Give the extent of all uninfected red blood cells.
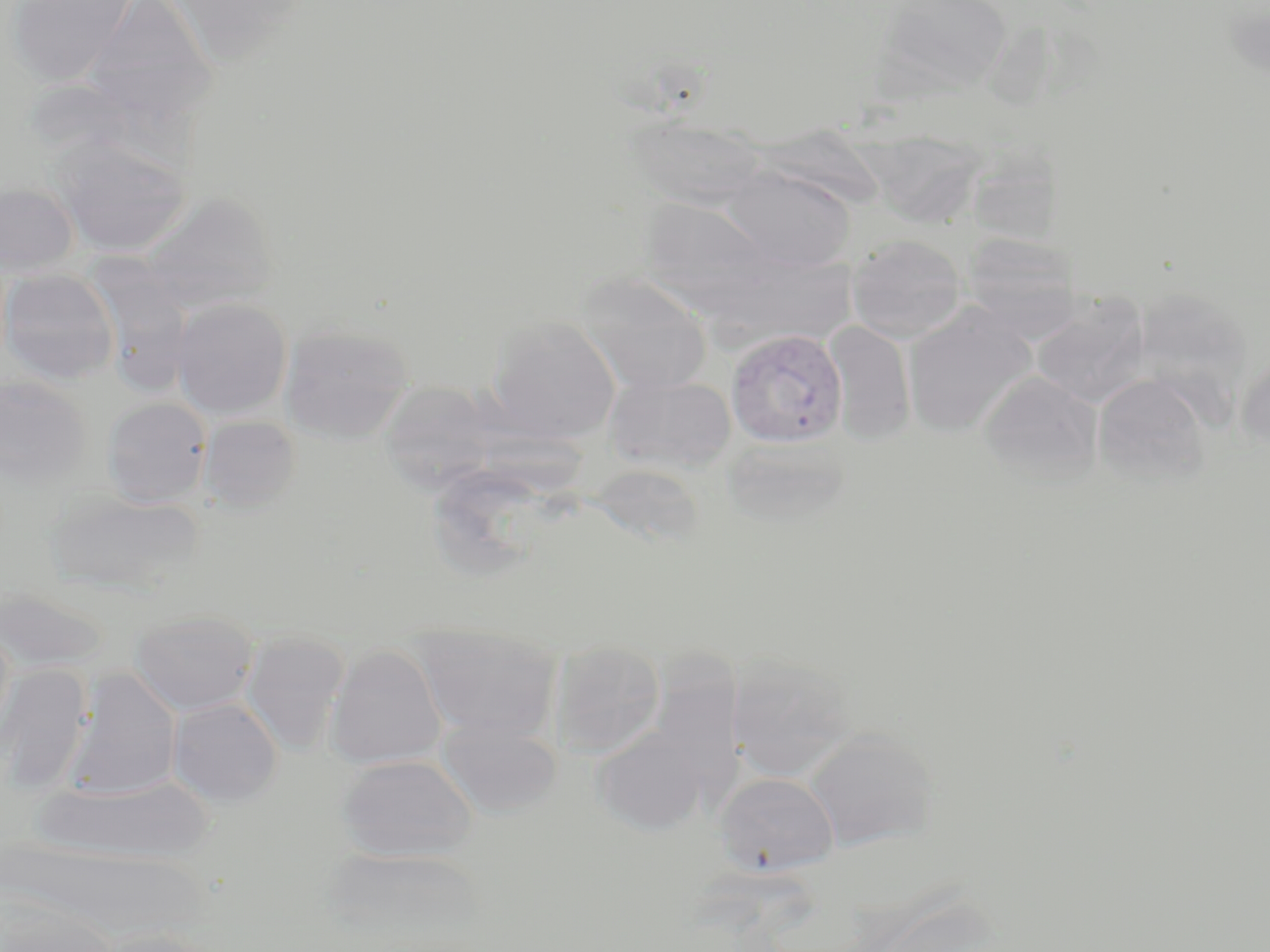
Approximate bounding boxes as [x1, y1, x2, y2] in pixels.
Uninfected red blood cells: [7, 0, 138, 87], [83, 0, 219, 125], [165, 0, 309, 65], [875, 0, 1014, 96], [626, 115, 769, 210], [49, 133, 191, 256], [867, 134, 984, 233], [966, 145, 1065, 246], [718, 164, 857, 273], [0, 182, 79, 276], [139, 191, 278, 314], [646, 203, 785, 327], [961, 231, 1084, 338], [847, 234, 967, 343], [96, 253, 205, 404], [0, 268, 119, 385], [574, 271, 713, 396], [1131, 286, 1253, 406], [1031, 295, 1150, 408], [171, 298, 292, 418], [902, 304, 1037, 436], [487, 315, 621, 443], [823, 322, 916, 444], [280, 323, 414, 443], [1235, 352, 1270, 455], [978, 370, 1103, 483], [603, 374, 736, 473], [1092, 374, 1210, 485], [0, 375, 92, 486], [379, 380, 496, 491], [101, 397, 212, 507], [199, 415, 301, 511], [721, 439, 853, 532], [45, 489, 203, 596], [0, 585, 109, 673], [131, 610, 259, 715], [0, 623, 16, 748], [414, 627, 561, 742], [242, 632, 349, 754], [550, 640, 665, 758], [324, 643, 447, 769], [725, 653, 856, 780], [0, 664, 91, 794], [65, 669, 182, 799], [169, 698, 283, 806], [436, 717, 562, 817], [591, 724, 711, 837], [803, 728, 939, 852], [338, 754, 476, 863], [715, 772, 838, 875], [34, 776, 215, 864], [320, 846, 492, 952], [0, 897, 118, 952], [89, 928, 224, 952].

Plasmodium vivax-infected red blood cell locations: [726, 328, 848, 448]. Slide-level diagnosis: Plasmodium vivax. Thin blood smear. May-Grünwald-Giemsa-stained preparation. Image is 1270×952 pixels. Captured at 1000x magnification. Single field of view. Light microscopy.